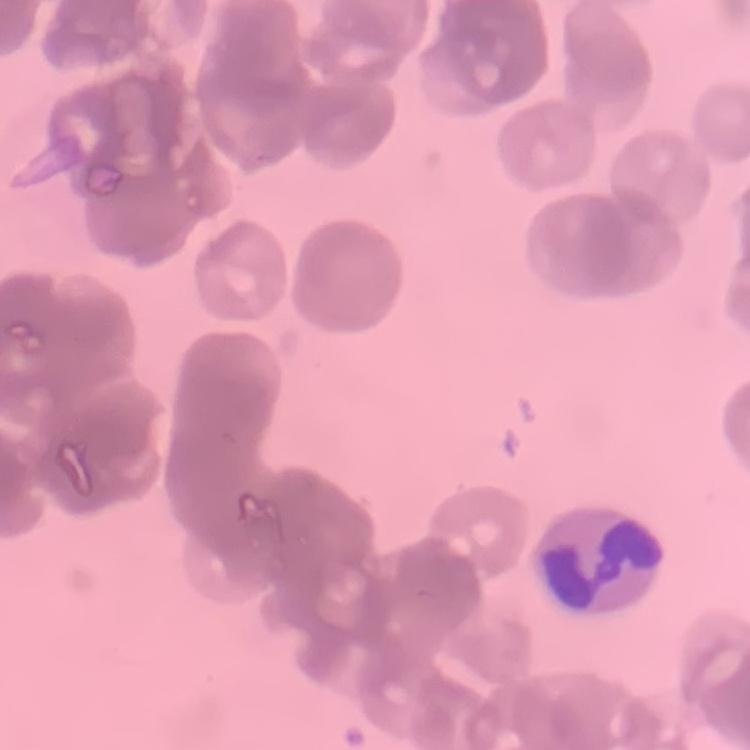 The red blood cells show rouleaux formation. One tile cut from a larger photomicrograph. Field's or Giemsa stain. Thin blood film.